Report the malaria status of this cell.
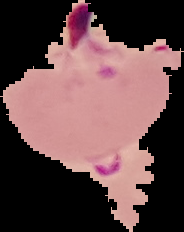

Parasitized.

Image is 184×232 pixels. Cell region segmented out of the field of view; the surrounding area is masked to black. From a thin blood smear.